Classify this cell by malaria status.
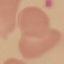
It is uninfected.

Summary:
  - Image type: automatically extracted cell patch, resized to 64 × 64 pixels
  - Preparation: thin blood film
  - Stain: Giemsa
  - Capture: smartphone through the microscope eyepiece